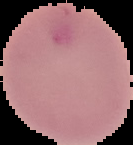
Summary:
  - Image type: segmented cell region with the area outside set to black
  - Result: no malaria parasites detected
  - Image size: 133×145 pixels
  - Preparation: thin blood smear